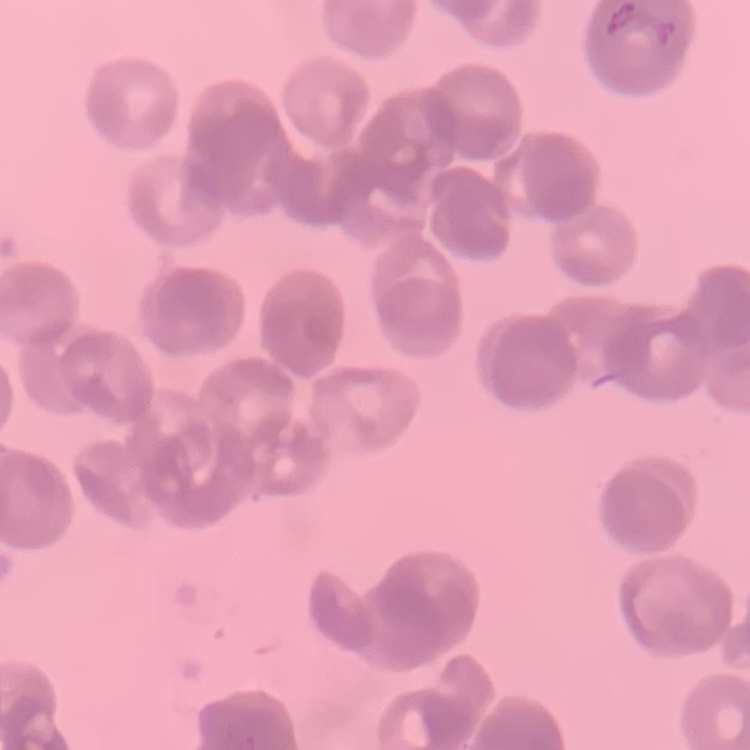 The red blood cells show rouleaux formation. Field's or Giemsa stain. Thin peripheral smear. Square crop of a larger photomicrograph.